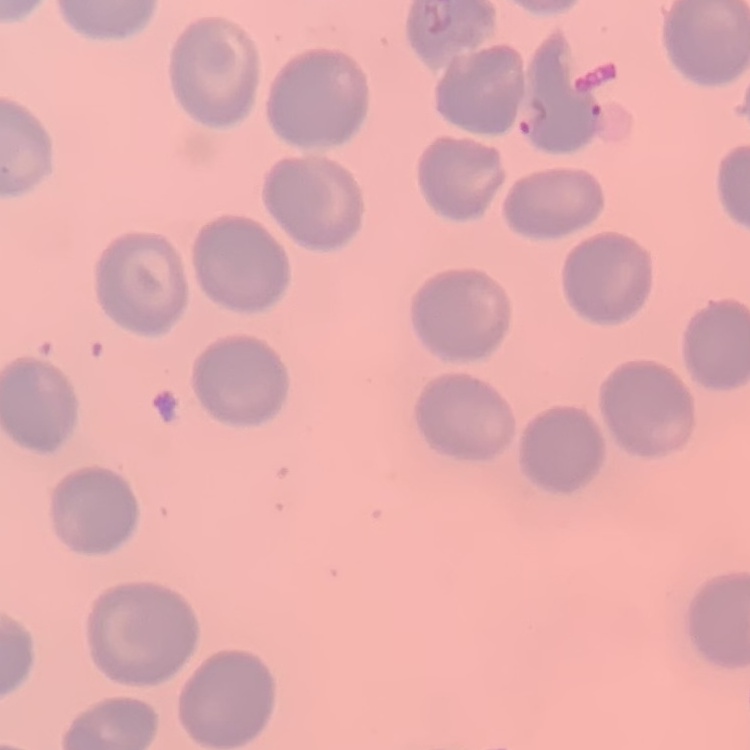

Summary:
  - Erythrocyte morphology: no rouleaux formation
  - Preparation: thin blood film
  - Image type: one tile cut from a larger photomicrograph
  - Stain: Field's or Giemsa